Assess the morphology of the red blood cells.
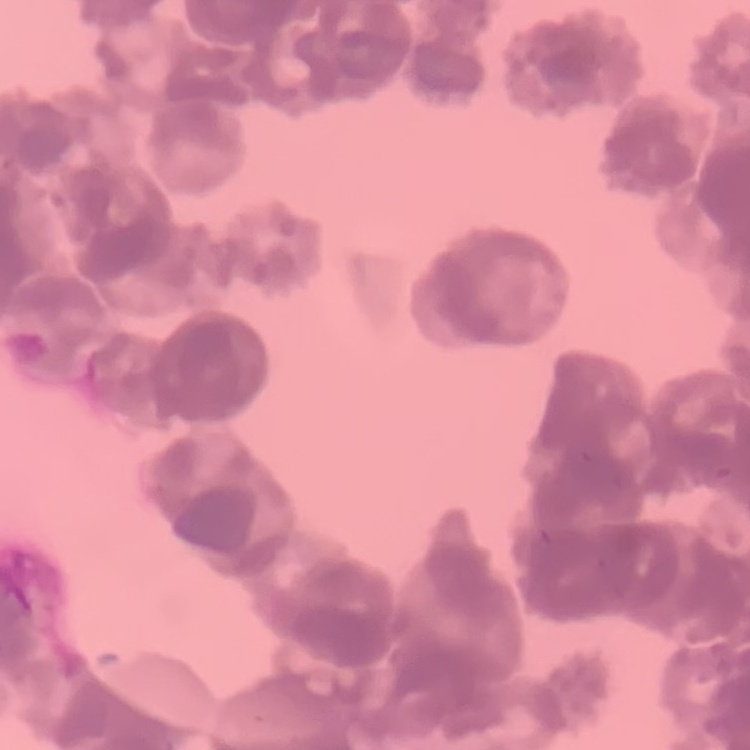
They show rouleaux formation.

stain = Field's or Giemsa
image type = square crop of a larger photomicrograph
preparation = thin peripheral smear